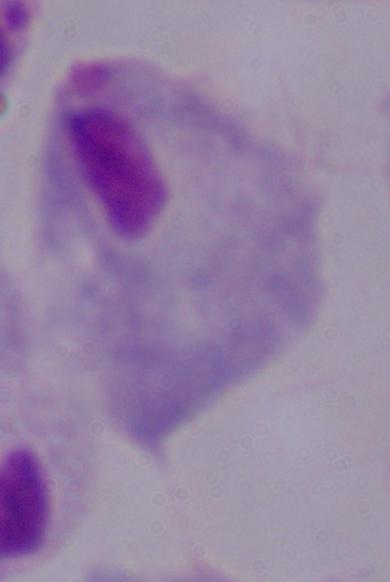

Micrograph. A trichomonad is seen. Captured at 1000x magnification.